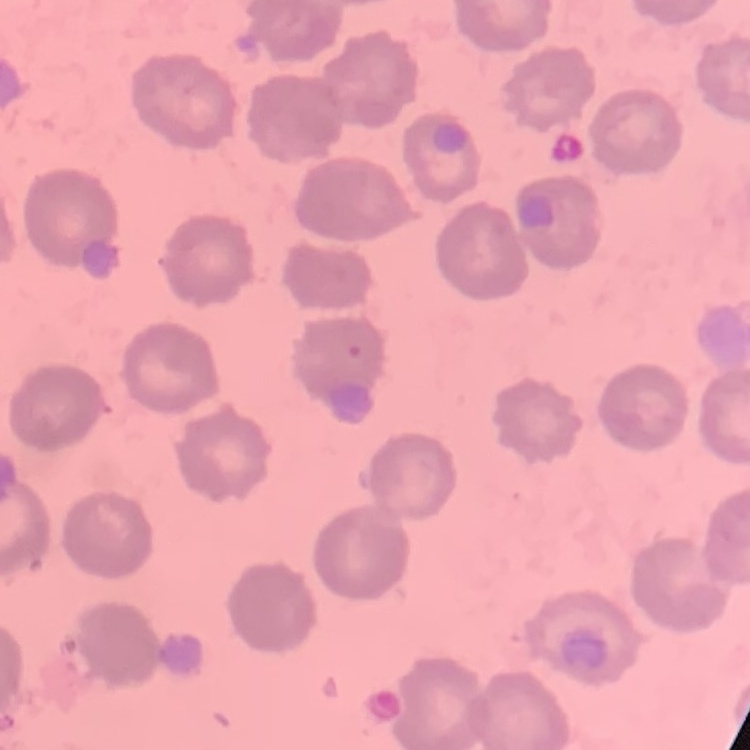

Summary:
  - Erythrocyte morphology: no rouleaux formation
  - Stain: Field's or Giemsa
  - Image type: square crop of a larger photomicrograph
  - Preparation: thin peripheral smear